Give the extent of all Plasmodium falciparum-infected red blood cells.
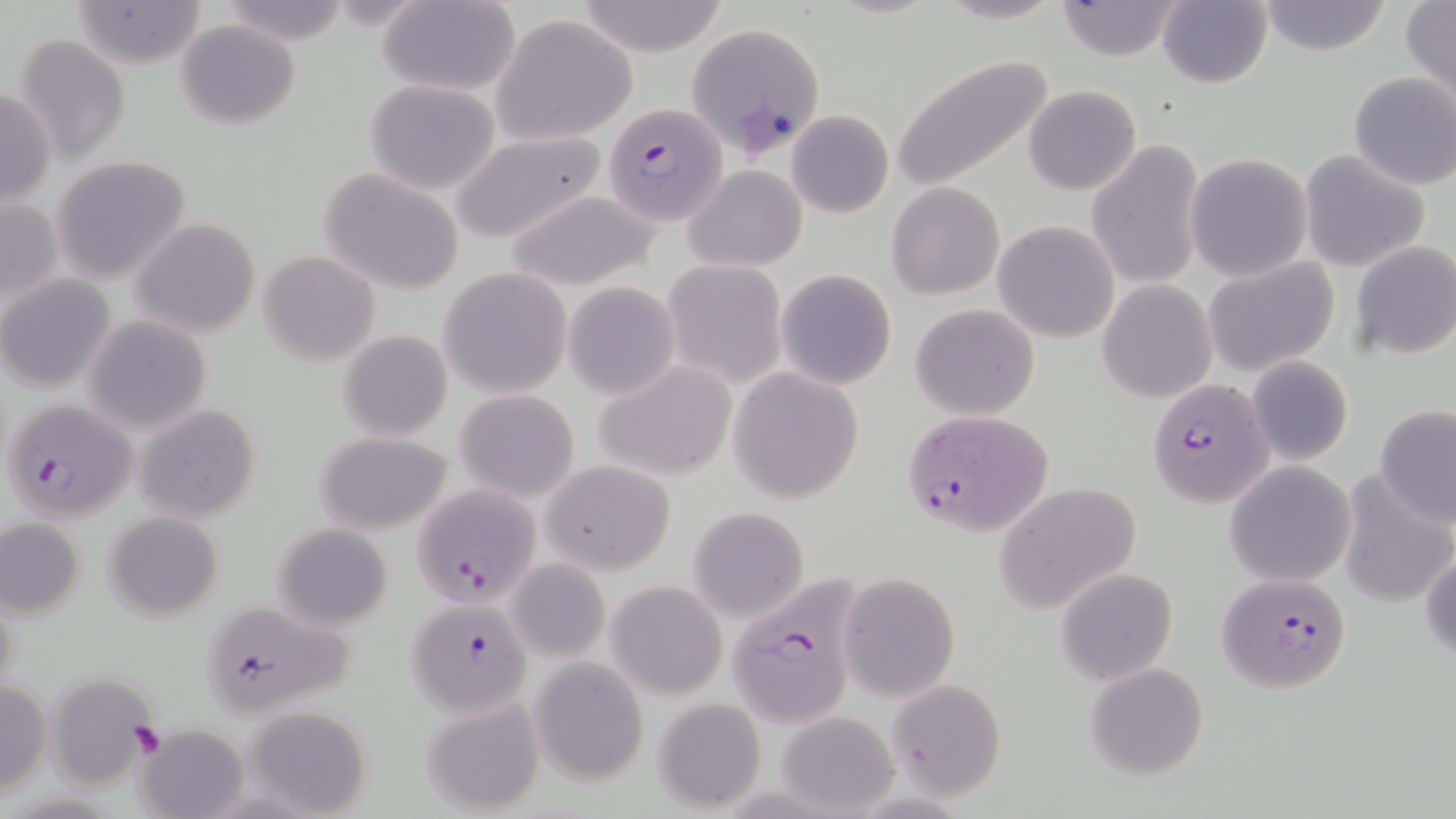
Approximate bounding boxes as [x1, y1, x2, y2] in pixels.
Plasmodium falciparum-infected red blood cells: [684, 22, 827, 161], [603, 103, 726, 225], [1150, 382, 1269, 508], [4, 397, 137, 523], [902, 408, 1054, 540], [411, 483, 541, 608], [1216, 571, 1353, 695], [723, 579, 863, 728], [198, 598, 360, 719], [406, 599, 531, 721].

slide-level diagnosis = Plasmodium falciparum
image size = 1456×819 pixels
stain = May-Grünwald-Giemsa
preparation = thin blood smear
platelet locations = approximate bounding boxes as [x1, y1, x2, y2] in pixels: [129, 723, 167, 760]
uninfected red blood cell locations = approximate bounding boxes as [x1, y1, x2, y2] in pixels: [216, 0, 350, 44], [933, 0, 1067, 24], [1256, 0, 1394, 56], [67, 1, 207, 68], [376, 1, 521, 96], [1053, 1, 1188, 62], [1156, 1, 1273, 88], [574, 2, 730, 56], [1401, 2, 1456, 101], [491, 15, 636, 145], [175, 19, 301, 130], [11, 34, 133, 165], [889, 55, 1056, 193], [1347, 71, 1456, 191], [363, 81, 502, 196], [1024, 85, 1142, 196], [0, 87, 56, 208], [1049, 96, 1175, 244], [787, 109, 893, 219], [448, 131, 606, 243], [1086, 140, 1206, 295], [1299, 150, 1431, 274], [1186, 153, 1312, 281], [54, 156, 190, 284], [682, 165, 806, 273], [318, 167, 465, 295], [886, 182, 1005, 299], [500, 189, 668, 291], [0, 195, 63, 316], [129, 217, 259, 339], [993, 221, 1120, 344], [1350, 240, 1456, 361], [258, 251, 379, 364], [1202, 257, 1341, 377], [661, 260, 789, 389], [436, 267, 573, 398], [775, 268, 897, 391], [2, 276, 116, 391], [1098, 280, 1216, 402], [563, 281, 680, 399], [909, 303, 1041, 420], [84, 315, 212, 435], [336, 330, 453, 441], [1246, 356, 1353, 466], [595, 358, 738, 481], [726, 367, 866, 504], [455, 388, 581, 501], [133, 403, 259, 524], [1374, 406, 1455, 527], [314, 431, 453, 533], [542, 460, 677, 574], [1224, 461, 1357, 588], [1335, 471, 1454, 607], [995, 481, 1141, 615], [686, 506, 810, 624], [102, 509, 224, 621], [1, 519, 86, 619], [272, 522, 394, 631], [1419, 548, 1456, 662], [506, 559, 609, 661], [1054, 567, 1179, 685], [839, 573, 959, 701], [605, 582, 728, 699], [1, 585, 20, 702], [531, 657, 649, 787], [1085, 663, 1209, 780], [45, 671, 157, 790], [886, 680, 1009, 802], [0, 681, 51, 795], [421, 695, 547, 816], [653, 698, 768, 813], [243, 705, 371, 818], [775, 711, 899, 814], [139, 729, 249, 819]
magnification = 1000x
field of view = single
modality = optical microscopy